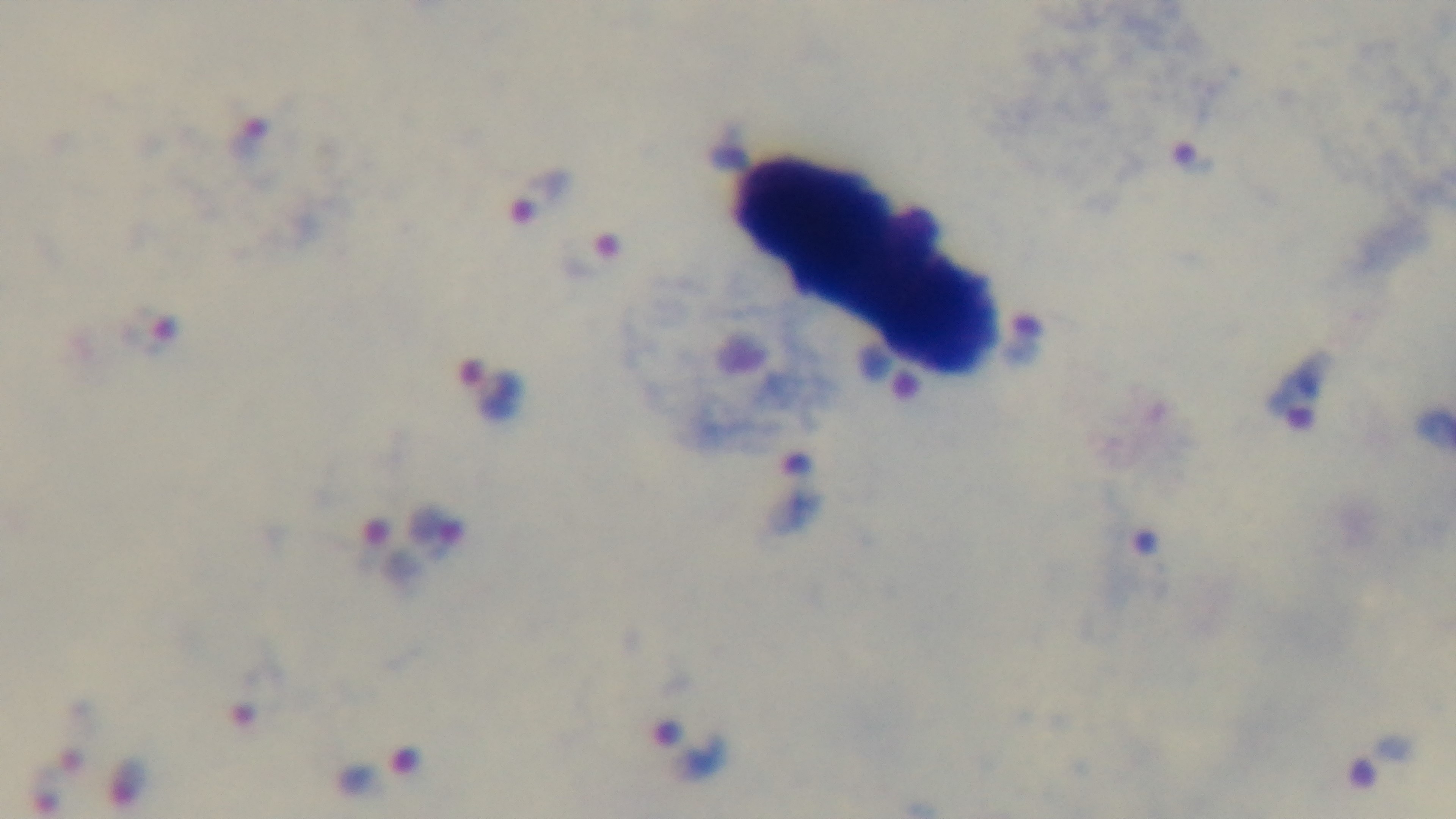

Photomicrograph. Malaria status: infected. 100x oil-immersion objective. One field from the slide. Captured with a mounted 4K digital camera. Preparation: thick. Giemsa-stained.